Give the position of every malaria parasite.
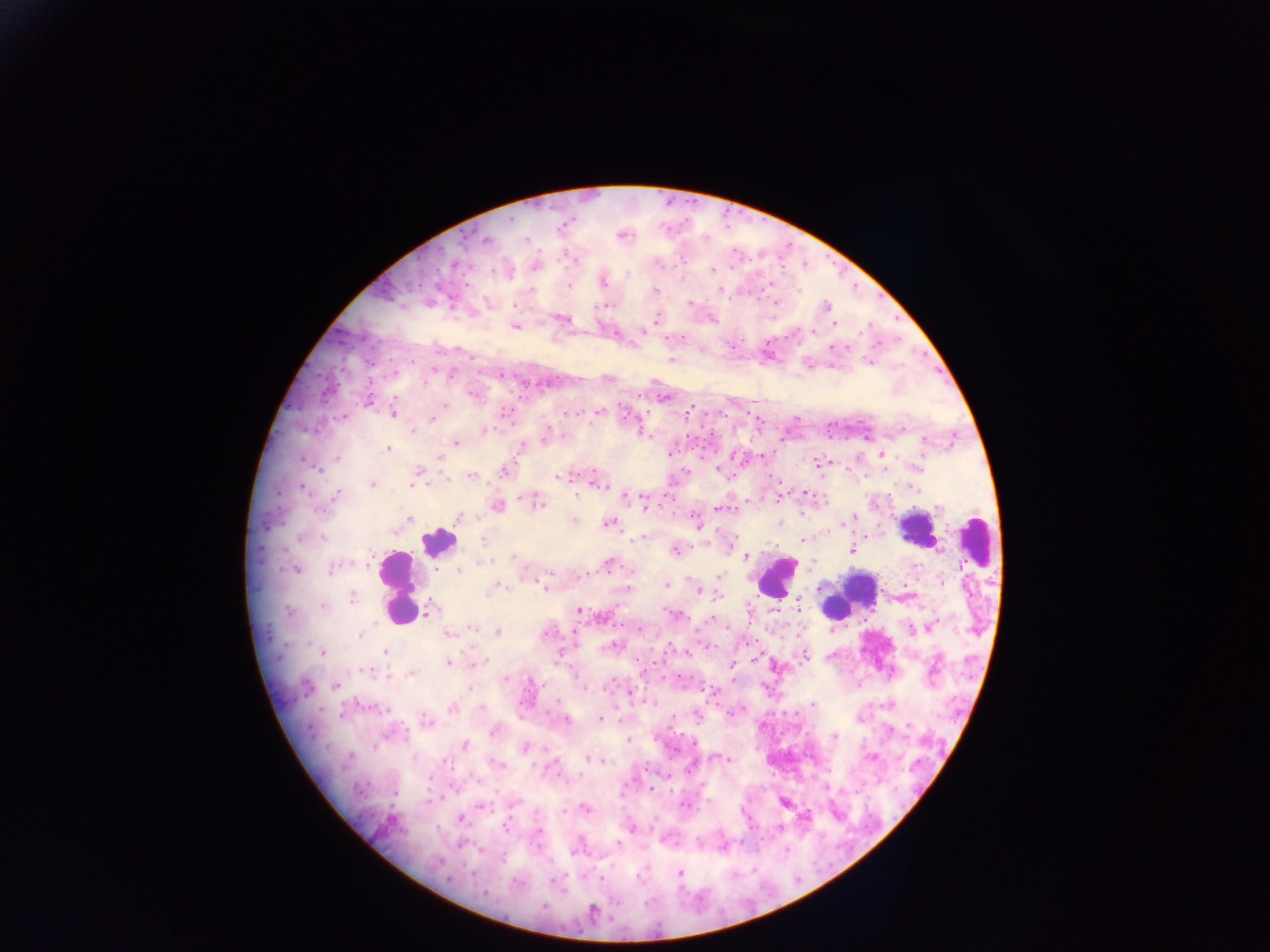
Approximate centers as x y in pixels.
Malaria parasites: 562 225; 622 234; 487 240; 572 257; 536 265; 711 270; 602 280; 568 284; 719 290; 654 291; 775 304; 604 305; 691 305; 826 306; 562 318; 656 318; 834 322; 515 326; 831 347; 703 350; 670 360; 869 361; 434 368; 500 374; 606 377; 472 393; 663 397; 368 400; 599 410; 688 411; 393 413; 504 413; 573 413; 434 415; 625 416; 344 417; 412 430; 484 430; 546 435; 456 441; 924 442; 388 449; 669 454; 880 454; 336 458; 440 458; 819 463; 504 469; 418 473; 471 475; 563 476; 446 480; 598 482; 372 484; 910 486; 337 494; 627 496; 808 496; 643 498; 538 502; 497 506; 719 507; 409 518; 457 518; 695 518; 851 518; 574 521; 609 523; 640 537; 803 540; 674 549; 851 550; 745 556; 608 564; 333 567; 436 567; 294 568; 719 576; 495 585; 666 585; 546 587; 698 589; 627 590; 902 596; 351 597; 797 605; 322 606; 427 610; 578 610; 750 613; 675 615; 928 627; 496 631; 447 633; 614 646; 321 652; 384 652; 686 653; 559 655; 804 655; 448 662; 474 663; 732 663; 775 666; 365 670; 411 673; 304 686; 334 686; 714 692; 630 693; 557 702; 451 708; 599 718; 618 719; 564 720; 425 722; 908 725; 495 730; 834 736; 628 740; 464 745; 524 747; 729 757; 872 757; 588 758; 496 763; 651 789; 512 802; 784 802; 480 805; 683 805; 584 809; 460 820; 630 826; 505 827; 680 873; 554 880; 592 912.

Leukocyte locations: 917 527; 977 541; 438 542; 776 576; 398 588; 847 596. Collected in Ghana. Thick blood smear. Image is 1270×952 pixels. Photographed through a microscope with a mobile-phone camera. Single field of view.